Outline each blood parasite and name the species.
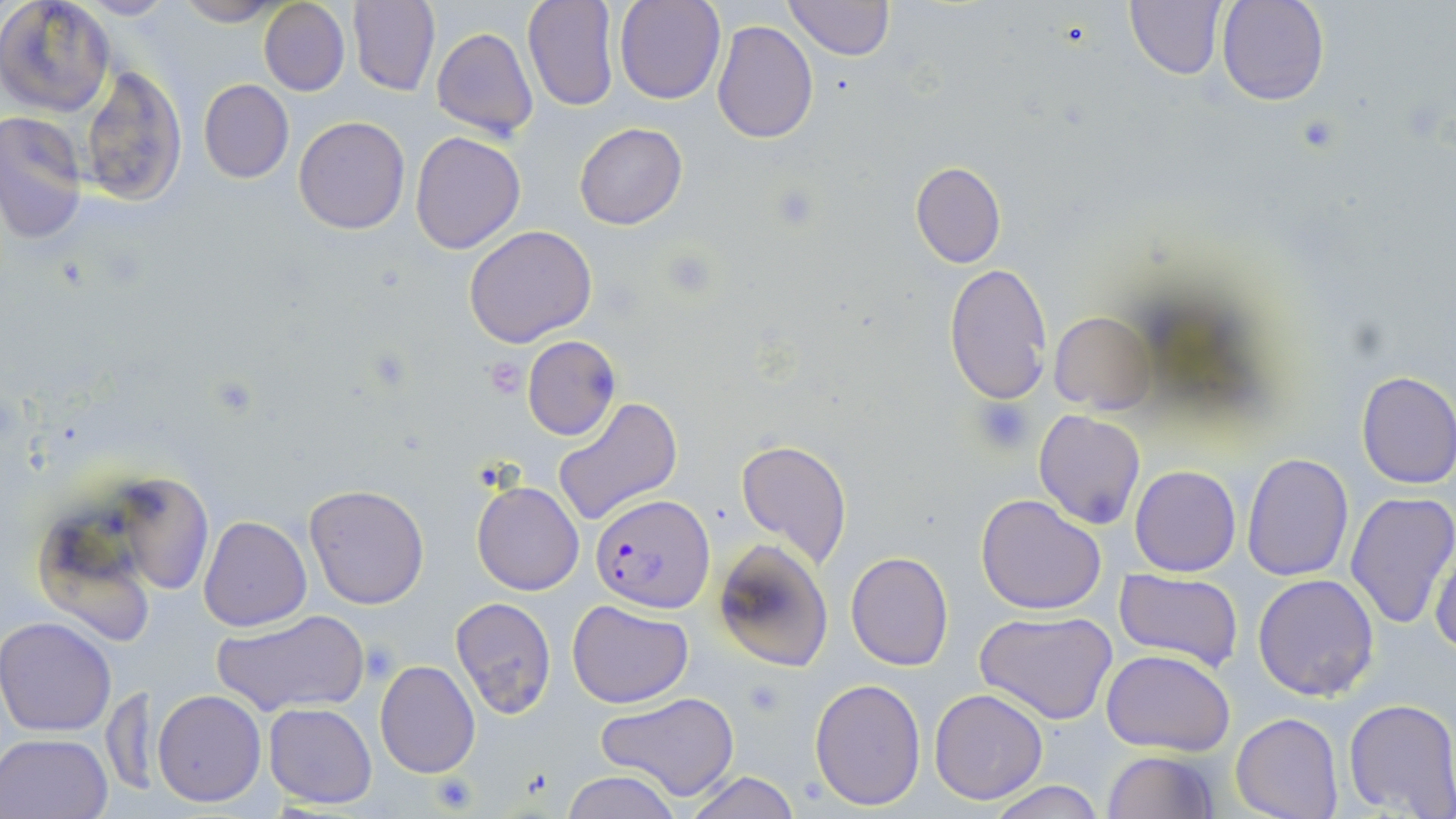
Approximate bounding boxes as (x1,y1)-(x2,y2) corner pairs in pixels.
Plasmodium falciparum-infected red blood cells: (589,493)-(715,610).
No Plasmodium ovale, Plasmodium malariae, Plasmodium vivax, Babesia divergens, or Trypanosoma brucei observed.

slide-level diagnosis = Plasmodium falciparum
modality = light microscopy
image size = 1456×819 pixels
stain = May-Grünwald-Giemsa
field of view = single
platelet locations = approximate bounding boxes as (x1,y1)-(x2,y2) corner pairs in pixels: (767,182)-(823,232), (483,356)-(528,399), (973,398)-(1037,452), (360,640)-(399,684), (741,674)-(788,719), (429,770)-(481,815)
uninfected red blood cell locations = approximate bounding boxes as (x1,y1)-(x2,y2) corner pairs in pixels: (76,0)-(173,20), (171,0)-(287,26), (521,0)-(619,111), (613,0)-(725,104), (785,0)-(893,60), (1124,0)-(1226,80), (1218,0)-(1328,105), (1,1)-(117,118), (259,1)-(350,96), (349,1)-(440,95), (711,18)-(820,144), (431,28)-(539,141), (80,66)-(187,207), (198,80)-(294,183), (1,111)-(90,245), (294,116)-(411,235), (574,123)-(688,230), (410,131)-(526,255), (910,161)-(1006,268), (463,225)-(598,347), (943,262)-(1052,404), (1050,312)-(1157,412), (521,335)-(620,440), (1354,370)-(1456,489), (551,396)-(684,527), (1031,410)-(1145,531), (735,438)-(853,571), (1241,453)-(1353,582), (29,456)-(218,639), (1130,465)-(1241,576), (472,480)-(584,596), (303,484)-(431,611), (1345,491)-(1456,631), (975,493)-(1107,614), (199,515)-(311,632), (1401,526)-(1452,659), (712,539)-(834,672), (1429,541)-(1456,658), (845,551)-(954,672), (1114,570)-(1243,672), (1252,573)-(1380,701), (448,597)-(555,718), (567,599)-(692,709), (211,609)-(369,717), (973,611)-(1120,725), (0,616)-(120,737), (1103,648)-(1235,757), (374,660)-(480,780), (809,678)-(927,811), (928,688)-(1049,806), (104,689)-(160,795), (153,689)-(266,807), (597,692)-(740,802), (1343,698)-(1456,818), (264,703)-(378,809), (1231,713)-(1342,819), (0,732)-(111,818), (1102,750)-(1218,818), (683,770)-(802,819), (560,771)-(685,819), (985,780)-(1105,819)
magnification = 1000x
preparation = thin blood film